Name the parasite shown.
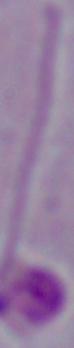
This is Leishmania.

modality = photomicrograph
magnification = 1000x